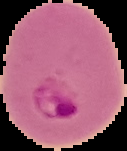

Summary:
  - Image type: segmented cell region on a black background
  - Image size: 127×151 pixels
  - Malaria status: parasitized
  - Preparation: thin blood film